Describe the morphology of the red blood cells.
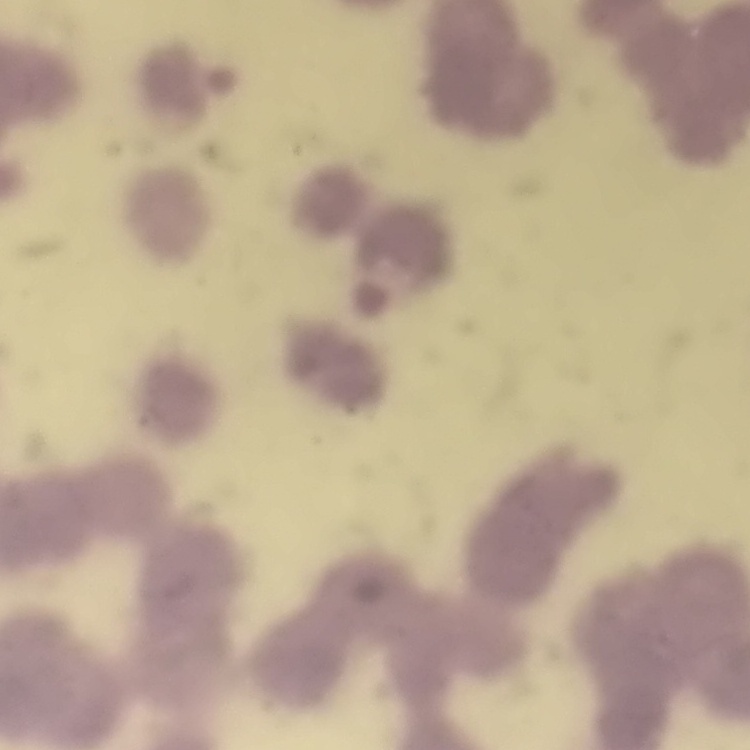
Rouleaux formation.

Thin blood film. Stained with either Field's or Giemsa. Square crop of a larger photomicrograph.